Outline each uninfected red blood cell.
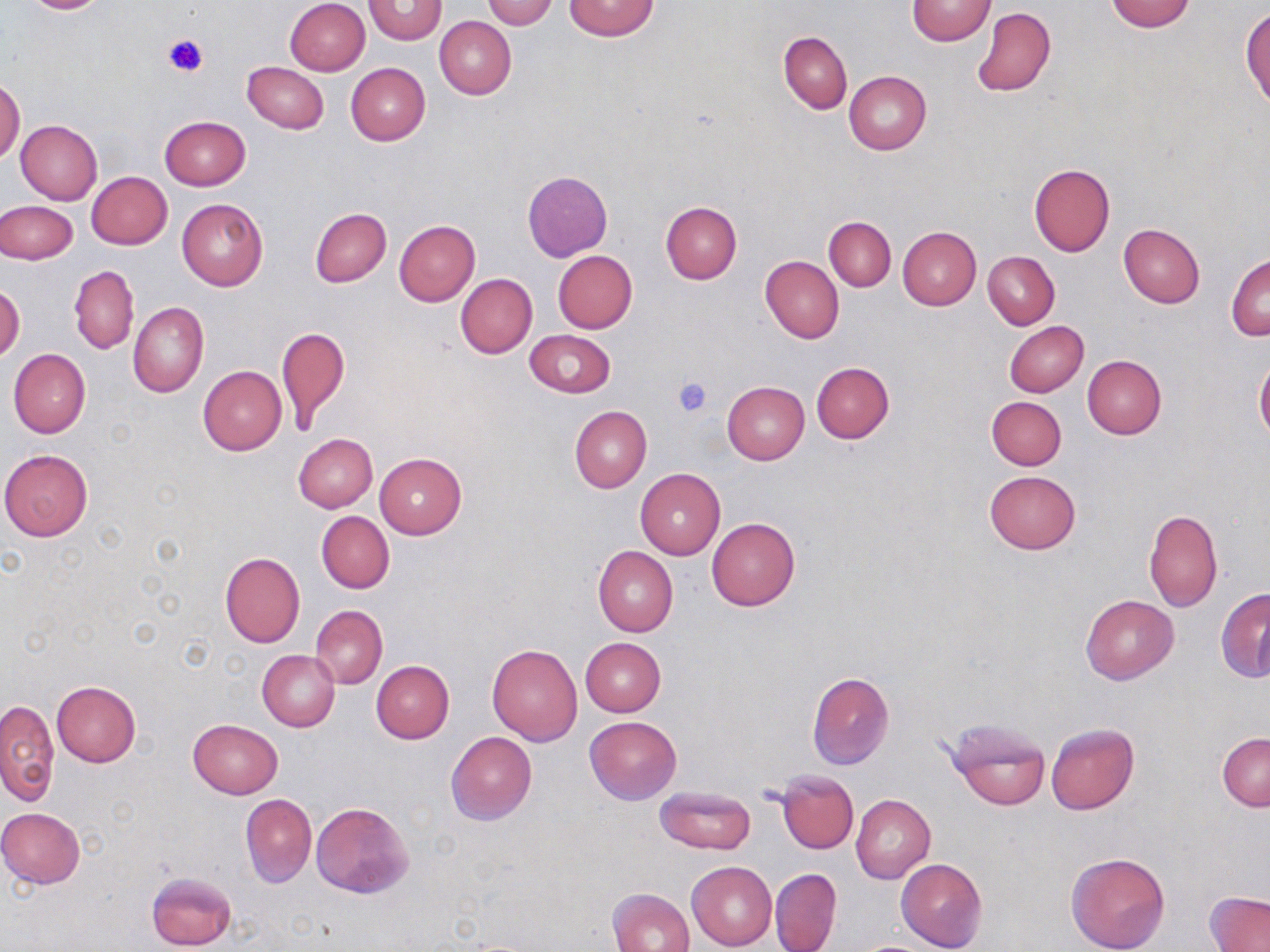

Approximate bounding boxes as (x1, y1, x2, y2) in pixels.
Uninfected red blood cells: (20, 0, 113, 15), (285, 0, 370, 76), (363, 0, 446, 44), (484, 0, 557, 28), (563, 0, 660, 41), (908, 0, 994, 44), (1104, 0, 1197, 32), (972, 7, 1055, 96), (1242, 8, 1270, 108), (434, 17, 515, 99), (779, 32, 852, 113), (243, 62, 328, 134), (345, 62, 430, 145), (844, 70, 930, 154), (0, 78, 24, 164), (159, 116, 251, 191), (16, 120, 102, 206), (1027, 163, 1115, 257), (522, 171, 612, 262), (86, 172, 172, 249), (177, 198, 268, 290), (1, 200, 77, 263), (661, 202, 742, 283), (310, 208, 391, 287), (825, 215, 896, 291), (393, 220, 480, 306), (1118, 224, 1205, 308), (898, 226, 981, 310), (553, 250, 637, 334), (984, 251, 1059, 329), (1227, 254, 1269, 341), (760, 256, 843, 343), (69, 265, 139, 354), (456, 274, 537, 358), (0, 286, 23, 363), (129, 302, 208, 398), (1004, 321, 1088, 398), (999, 323, 1078, 470), (277, 324, 349, 435), (525, 329, 615, 397), (8, 349, 91, 438), (1082, 354, 1167, 439), (1255, 357, 1270, 441), (811, 362, 894, 443), (199, 365, 286, 454), (722, 381, 810, 464), (986, 396, 1066, 470), (569, 405, 652, 493), (293, 433, 377, 512), (1, 449, 93, 540), (374, 452, 466, 539), (636, 468, 725, 559), (984, 470, 1080, 554), (1144, 509, 1223, 611), (317, 511, 394, 593), (707, 518, 800, 611), (592, 546, 678, 636), (221, 552, 305, 648), (1216, 589, 1270, 682), (1081, 594, 1179, 685), (311, 606, 387, 688), (580, 638, 666, 717), (488, 644, 583, 746), (257, 650, 339, 731), (372, 661, 454, 743), (806, 672, 895, 770), (51, 681, 141, 767), (1, 698, 58, 806), (584, 716, 681, 804), (946, 717, 1050, 810), (188, 719, 282, 799), (1046, 723, 1138, 815), (446, 732, 537, 825), (1218, 733, 1270, 810), (775, 769, 859, 854), (654, 786, 756, 855), (241, 794, 317, 886), (851, 794, 935, 883), (310, 802, 413, 899), (1, 808, 86, 889), (1066, 852, 1170, 952), (895, 857, 987, 952), (686, 861, 777, 949), (769, 868, 842, 952), (146, 869, 237, 951), (609, 887, 695, 952), (1206, 891, 1269, 952).

Platelet locations: (164, 34, 208, 78), (673, 376, 714, 418). Slide-level diagnosis: negative for blood parasites. Thin blood smear. Captured at 1000x magnification. Image is 1270×952 pixels. Light microscopy. One field of a larger specimen. May-Grünwald-Giemsa-stained preparation.